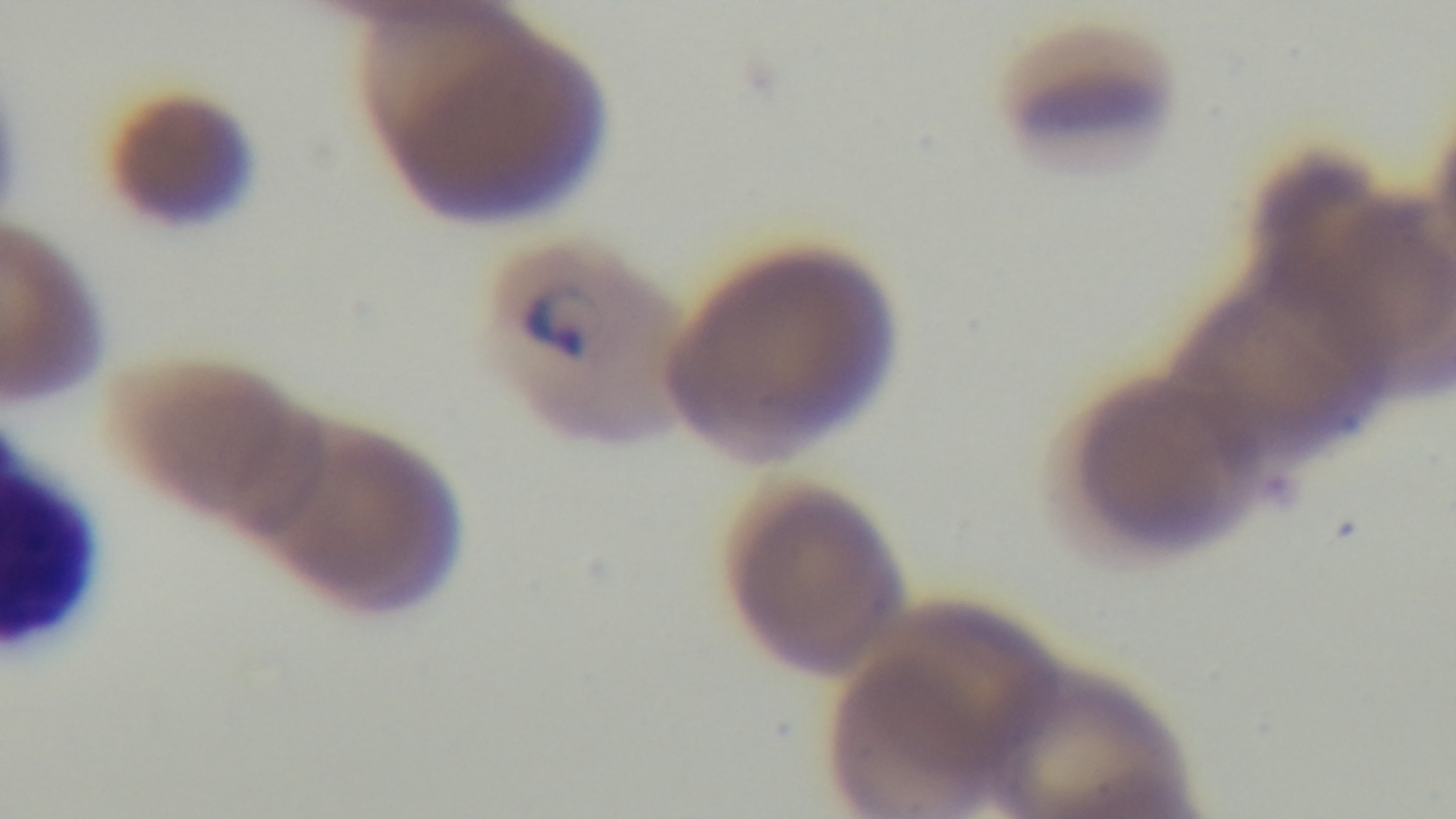
Captured with a mounted 4K digital camera. Giemsa-stained. Malaria status: infected. Single field of view. 100x oil-immersion objective. Preparation: thin. Light microscopy.